Mark where platelets are.
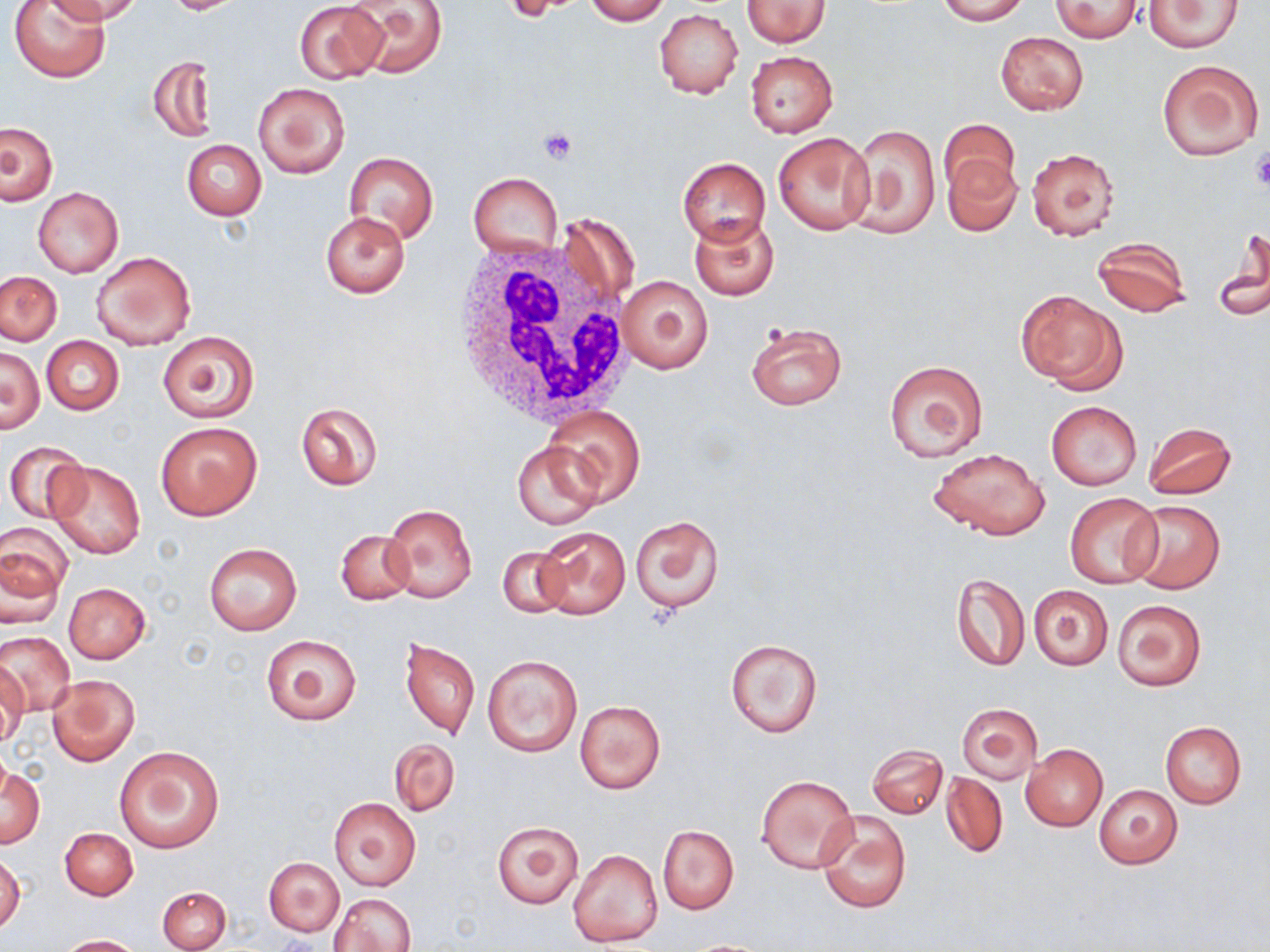

Approximate bounding boxes as named x1/y1/x2/y2 corners in pixels.
Platelets: (x1=538, y1=127, x2=578, y2=165), (x1=1250, y1=151, x2=1270, y2=192).

White blood cell locations: (x1=446, y1=234, x2=633, y2=428). Uninfected red blood cell locations: (x1=10, y1=0, x2=109, y2=81), (x1=57, y1=0, x2=143, y2=24), (x1=167, y1=0, x2=235, y2=14), (x1=583, y1=0, x2=671, y2=24), (x1=742, y1=0, x2=830, y2=47), (x1=936, y1=0, x2=1027, y2=24), (x1=1050, y1=0, x2=1145, y2=42), (x1=293, y1=1, x2=387, y2=83), (x1=346, y1=1, x2=448, y2=77), (x1=1143, y1=1, x2=1243, y2=52), (x1=655, y1=9, x2=743, y2=99), (x1=995, y1=31, x2=1089, y2=115), (x1=744, y1=51, x2=838, y2=137), (x1=149, y1=55, x2=216, y2=142), (x1=1156, y1=58, x2=1265, y2=160), (x1=253, y1=80, x2=350, y2=178), (x1=938, y1=118, x2=1021, y2=202), (x1=0, y1=122, x2=58, y2=204), (x1=847, y1=124, x2=940, y2=238), (x1=772, y1=133, x2=876, y2=236), (x1=181, y1=140, x2=266, y2=220), (x1=1025, y1=147, x2=1120, y2=240), (x1=343, y1=151, x2=439, y2=244), (x1=943, y1=155, x2=1022, y2=235), (x1=678, y1=158, x2=770, y2=243), (x1=468, y1=172, x2=563, y2=257), (x1=33, y1=187, x2=123, y2=278), (x1=555, y1=210, x2=641, y2=319), (x1=320, y1=211, x2=410, y2=296), (x1=689, y1=213, x2=780, y2=301), (x1=1214, y1=227, x2=1270, y2=322), (x1=1090, y1=236, x2=1191, y2=317), (x1=92, y1=250, x2=196, y2=350), (x1=1, y1=271, x2=62, y2=345), (x1=616, y1=274, x2=715, y2=375), (x1=1016, y1=289, x2=1126, y2=391), (x1=746, y1=321, x2=846, y2=411), (x1=158, y1=332, x2=259, y2=422), (x1=41, y1=336, x2=124, y2=416), (x1=1, y1=346, x2=44, y2=434), (x1=884, y1=360, x2=988, y2=462), (x1=1046, y1=401, x2=1142, y2=489), (x1=295, y1=402, x2=383, y2=490), (x1=543, y1=405, x2=646, y2=504), (x1=156, y1=420, x2=262, y2=521), (x1=1143, y1=422, x2=1238, y2=500), (x1=513, y1=439, x2=604, y2=530), (x1=4, y1=441, x2=88, y2=523), (x1=928, y1=448, x2=1050, y2=540), (x1=47, y1=460, x2=146, y2=558), (x1=1064, y1=493, x2=1162, y2=589), (x1=1124, y1=500, x2=1226, y2=593), (x1=381, y1=503, x2=477, y2=604), (x1=631, y1=515, x2=724, y2=614), (x1=1, y1=520, x2=76, y2=598), (x1=535, y1=526, x2=630, y2=620), (x1=335, y1=530, x2=414, y2=606), (x1=205, y1=543, x2=301, y2=635), (x1=497, y1=547, x2=571, y2=619), (x1=1, y1=548, x2=66, y2=628), (x1=952, y1=574, x2=1028, y2=672), (x1=64, y1=582, x2=151, y2=663), (x1=1028, y1=584, x2=1114, y2=670), (x1=1112, y1=599, x2=1207, y2=692), (x1=1, y1=631, x2=74, y2=717), (x1=261, y1=633, x2=361, y2=726), (x1=398, y1=635, x2=480, y2=741), (x1=723, y1=638, x2=823, y2=739), (x1=483, y1=655, x2=582, y2=757), (x1=0, y1=664, x2=28, y2=746), (x1=45, y1=673, x2=139, y2=767), (x1=575, y1=700, x2=665, y2=794), (x1=956, y1=702, x2=1043, y2=784), (x1=1161, y1=723, x2=1246, y2=807), (x1=388, y1=739, x2=459, y2=817), (x1=868, y1=744, x2=947, y2=819), (x1=1020, y1=744, x2=1108, y2=831), (x1=114, y1=745, x2=224, y2=854), (x1=0, y1=763, x2=45, y2=849), (x1=940, y1=771, x2=1007, y2=858), (x1=756, y1=775, x2=857, y2=874), (x1=1094, y1=785, x2=1183, y2=869), (x1=328, y1=798, x2=420, y2=891), (x1=816, y1=808, x2=912, y2=915), (x1=492, y1=820, x2=583, y2=909), (x1=658, y1=825, x2=739, y2=913), (x1=59, y1=826, x2=138, y2=900), (x1=567, y1=849, x2=662, y2=949), (x1=0, y1=852, x2=24, y2=934), (x1=265, y1=856, x2=344, y2=937), (x1=158, y1=886, x2=230, y2=951), (x1=331, y1=894, x2=416, y2=952), (x1=58, y1=935, x2=143, y2=952). Slide-level diagnosis: no evidence of blood parasites. Thin blood smear. May-Grünwald-Giemsa stain. Image is 1270×952 pixels. Captured at 1000x magnification. Optical microscopy. Single field of view.